Describe the morphology of the erythrocytes.
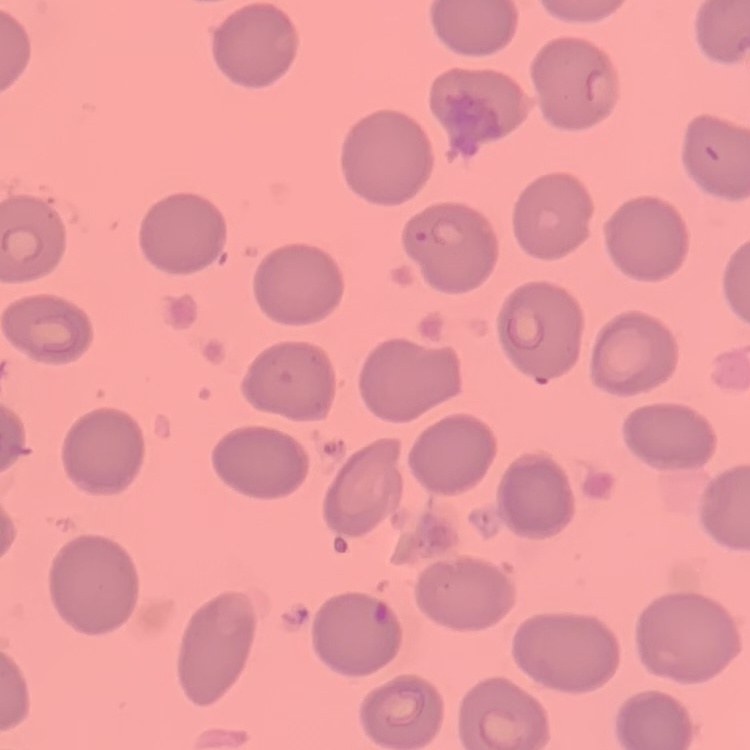
They show no rouleaux formation.

{
  "image_type": "square crop of a larger photomicrograph",
  "preparation": "thin peripheral smear",
  "stain": "Field's or Giemsa"
}